Classify this cell by malaria status.
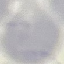
It is uninfected.

preparation = thin smear
capture = smartphone through the microscope eyepiece
image type = automatically extracted cell patch, resized to 64 × 64 pixels
stain = Giemsa